Describe the morphology of the erythrocytes.
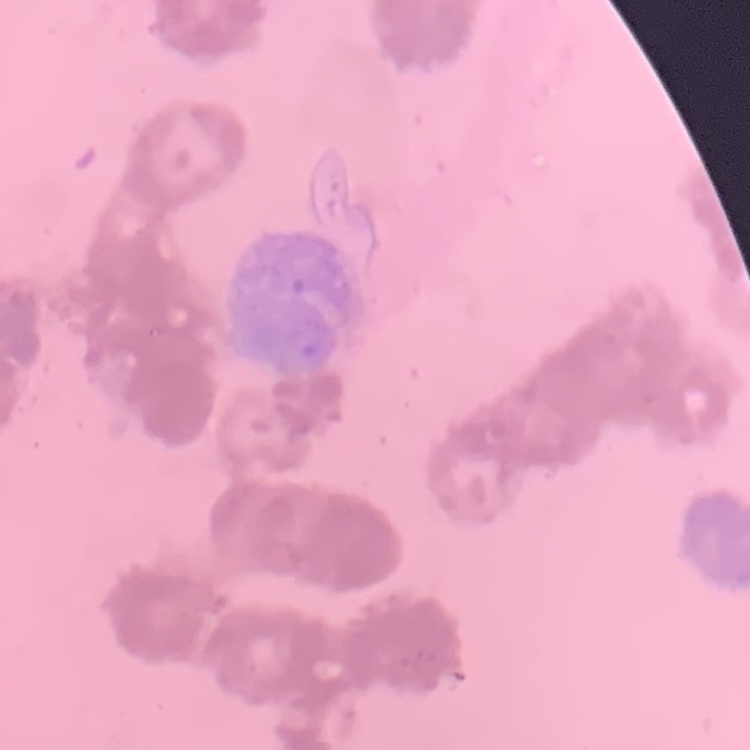

They show rouleaux formation.

{
  "stain": "Field's or Giemsa",
  "preparation": "thin blood film",
  "image_type": "one tile cut from a larger photomicrograph"
}